Classify this cell by malaria status.
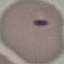

It is parasitized.

Summary:
  - Preparation: thin smear
  - Image type: automatically extracted cell patch, resized to 64 × 64 pixels
  - Capture: smartphone through the microscope eyepiece
  - Stain: Giemsa